Describe the morphology of the red blood cells.
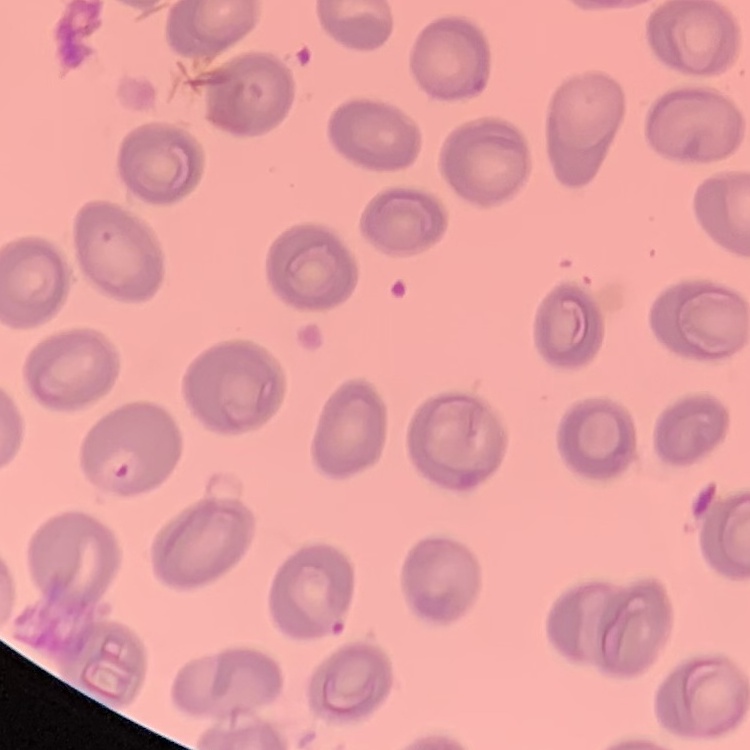
They show no rouleaux formation.

image type = square crop of a larger photomicrograph
preparation = thin blood film
stain = Field's or Giemsa